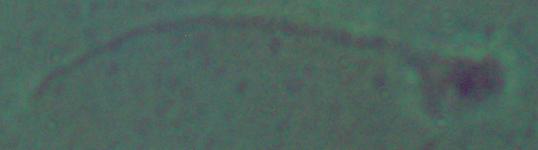

A Leishmania parasite is shown. 1000x magnification. Photomicrograph.